Locate every Plasmodium ovale-infected red blood cell.
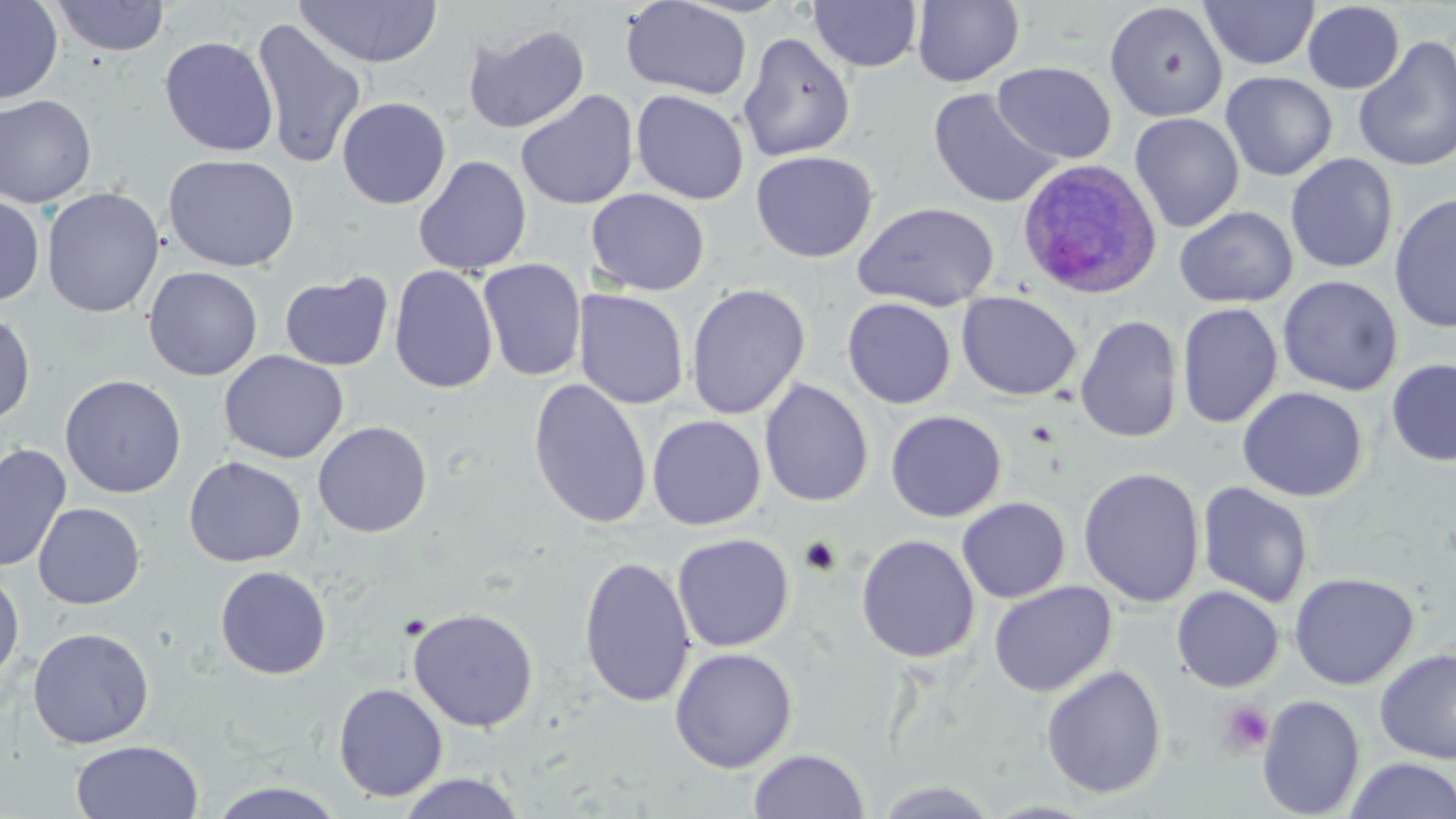
Approximate bounding boxes as [x1, y1, x2, y2] in pixels.
Plasmodium ovale-infected red blood cells: [1015, 158, 1162, 299].

Platelet locations: [1216, 700, 1276, 758]. Uninfected red blood cell locations: [50, 0, 171, 57], [808, 0, 923, 72], [911, 0, 1025, 87], [1199, 0, 1320, 71], [0, 1, 63, 105], [293, 1, 443, 68], [621, 1, 753, 101], [1104, 2, 1228, 122], [1302, 2, 1405, 94], [250, 18, 368, 169], [462, 22, 590, 134], [737, 32, 855, 162], [159, 35, 279, 157], [1352, 36, 1456, 173], [992, 61, 1116, 164], [1220, 71, 1338, 181], [928, 88, 1061, 210], [515, 89, 639, 210], [631, 89, 749, 205], [0, 94, 97, 208], [336, 97, 451, 210], [1130, 112, 1244, 232], [750, 150, 878, 262], [164, 153, 301, 272], [1285, 153, 1399, 273], [413, 156, 532, 275], [42, 187, 165, 318], [586, 189, 710, 295], [1388, 192, 1456, 334], [0, 194, 45, 307], [852, 202, 999, 312], [1174, 206, 1297, 308], [477, 258, 586, 381], [389, 265, 499, 395], [143, 266, 263, 381], [279, 271, 394, 371], [1278, 275, 1402, 396], [685, 283, 811, 420], [574, 289, 689, 409], [956, 291, 1082, 401], [842, 297, 956, 409], [1176, 302, 1283, 429], [0, 310, 36, 426], [1075, 315, 1183, 444], [219, 350, 348, 464], [1387, 358, 1456, 467], [60, 374, 187, 498], [527, 377, 652, 529], [759, 379, 874, 507], [1237, 386, 1367, 502], [885, 410, 1007, 522], [647, 415, 766, 530], [312, 421, 433, 538], [0, 443, 72, 573], [184, 456, 307, 567], [1078, 467, 1205, 608], [1196, 482, 1314, 609], [957, 497, 1071, 603], [33, 503, 145, 609], [672, 533, 795, 652], [856, 533, 979, 663], [578, 555, 695, 708], [214, 565, 332, 680], [0, 568, 25, 686], [1289, 571, 1419, 690], [988, 581, 1117, 697], [1171, 585, 1285, 692], [407, 606, 539, 732], [27, 626, 154, 749], [669, 646, 798, 773], [1374, 648, 1456, 765], [1040, 664, 1167, 799], [333, 682, 448, 803], [1257, 694, 1365, 818], [70, 740, 204, 819], [747, 748, 871, 818], [1343, 757, 1456, 818], [397, 772, 528, 818], [204, 780, 350, 819], [872, 780, 1003, 817]. Slide-level diagnosis: Plasmodium ovale. May-Grünwald-Giemsa stain. Light microscopy. Single field of view. 1000x magnification. Thin blood film. Image is 1456×819 pixels.